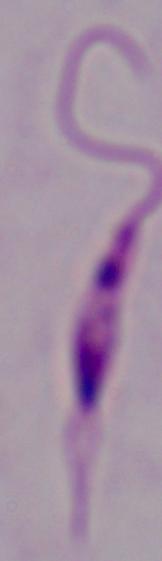

{
  "magnification": "1000x",
  "identification": "Leishmania",
  "modality": "micrograph"
}